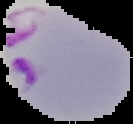

From a thin blood smear. The area outside the segmented cell region is set to black. Malaria status: parasitized. Image is 133×124 pixels.